Locate every white blood cell.
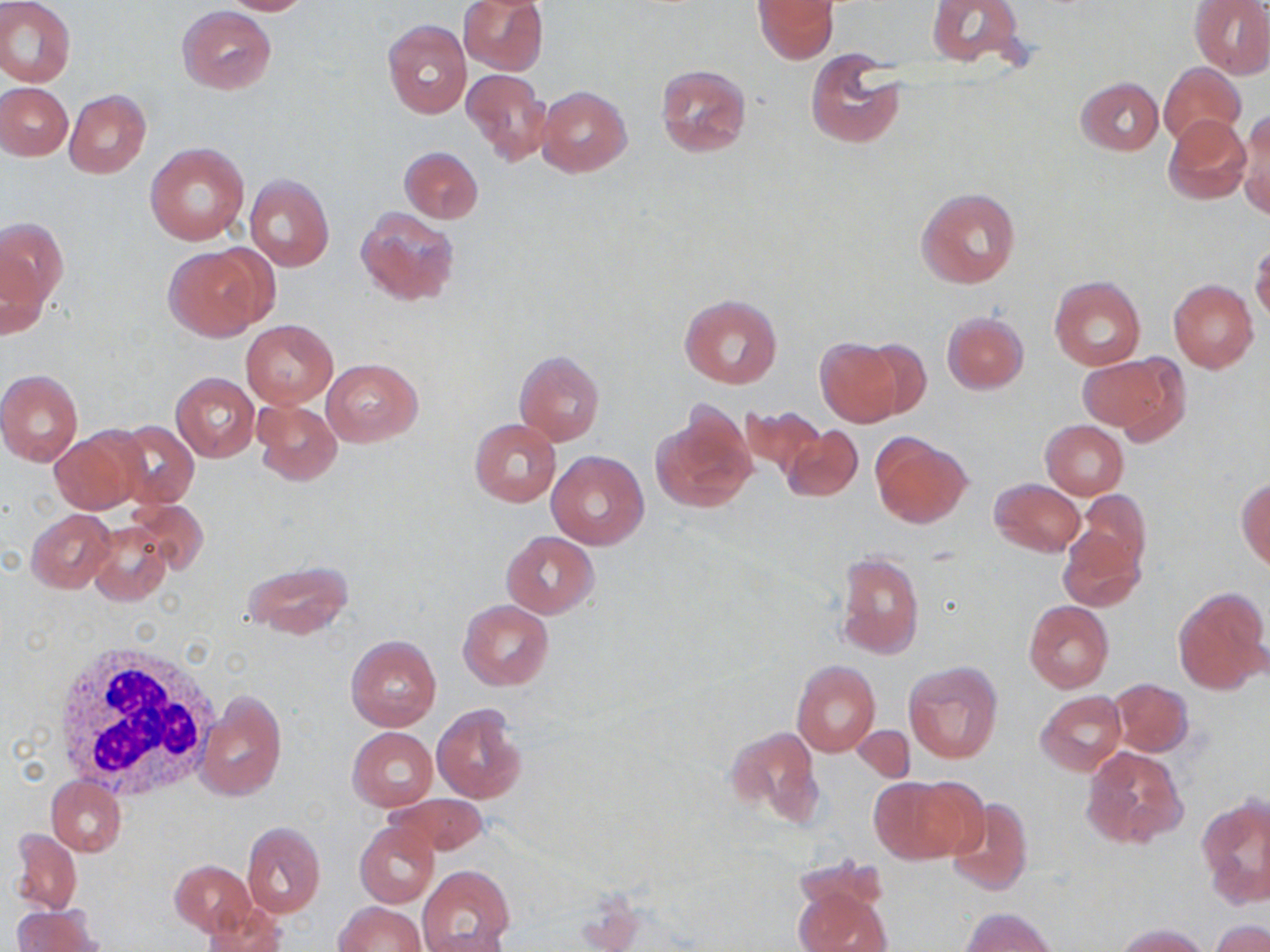
Approximate bounding boxes as (x1,y1)-(x2,y2) corner pairs in pixels.
White blood cells: (51,645)-(220,796).

Summary:
  - Uninfected red blood cell locations: (216,0)-(312,15), (458,0)-(549,75), (755,0)-(836,63), (926,0)-(1024,66), (1189,0)-(1270,78), (0,1)-(76,86), (177,6)-(276,94), (382,19)-(472,119), (805,50)-(904,148), (1158,62)-(1245,144), (655,64)-(751,157), (463,68)-(552,165), (1075,77)-(1163,155), (0,83)-(72,159), (535,85)-(632,176), (64,89)-(151,178), (1238,110)-(1270,217), (1165,114)-(1250,203), (147,143)-(249,246), (398,146)-(483,224), (244,174)-(335,274), (917,187)-(1020,288), (355,206)-(460,307), (0,216)-(66,316), (1251,241)-(1270,325), (162,245)-(272,341), (1049,275)-(1146,370), (1168,278)-(1258,373), (680,296)-(781,389), (942,312)-(1028,393), (242,319)-(337,407), (815,338)-(904,424), (857,339)-(933,421), (514,350)-(605,446), (1085,353)-(1189,444), (322,358)-(422,446), (0,369)-(84,465), (171,373)-(260,463), (252,400)-(342,485), (653,403)-(756,513), (737,405)-(827,480), (113,419)-(198,508), (469,420)-(561,506), (1040,421)-(1128,499), (49,426)-(147,515), (782,426)-(863,503), (871,434)-(971,529), (546,451)-(649,550), (1237,477)-(1270,571), (990,478)-(1084,556), (1077,488)-(1151,574), (130,499)-(208,575), (27,508)-(115,593), (88,519)-(171,607), (1058,524)-(1146,614), (501,530)-(599,619), (835,551)-(923,660), (243,560)-(353,639), (1172,588)-(1269,695), (458,600)-(553,691), (1023,600)-(1114,692), (346,635)-(441,731), (790,660)-(880,757), (904,661)-(1003,763), (1108,678)-(1194,756), (1036,690)-(1125,776), (197,691)-(287,802), (432,703)-(529,804), (852,726)-(915,780), (348,727)-(437,810), (727,727)-(823,827), (1080,745)-(1189,852), (46,775)-(126,855), (867,776)-(971,864), (388,792)-(490,855), (1197,794)-(1270,908), (945,797)-(1033,896), (355,820)-(440,908), (241,821)-(326,917), (10,829)-(82,915), (169,860)-(256,936), (418,865)-(514,951), (794,884)-(889,952), (199,901)-(287,952), (334,901)-(425,952), (12,905)-(103,952), (960,907)-(1056,951), (1208,919)-(1269,952), (1115,922)-(1212,951), (421,929)-(510,951)
  - Slide-level diagnosis: no evidence of blood parasites
  - Modality: light microscopy
  - Stain: May-Grünwald-Giemsa
  - Image size: 1270×952 pixels
  - Preparation: thin blood film
  - Field of view: single
  - Magnification: 1000x